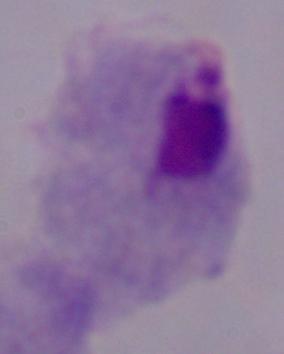

modality = micrograph
identification = trichomonad
magnification = 1000x